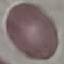
result: no malaria parasites detected
capture: smartphone camera at the microscope eyepiece
image_type: cell patch, automatically extracted from a larger field of view and resized to 64 × 64 pixels
stain: Giemsa
preparation: thin blood smear